Comment on the morphology of the red blood cells.
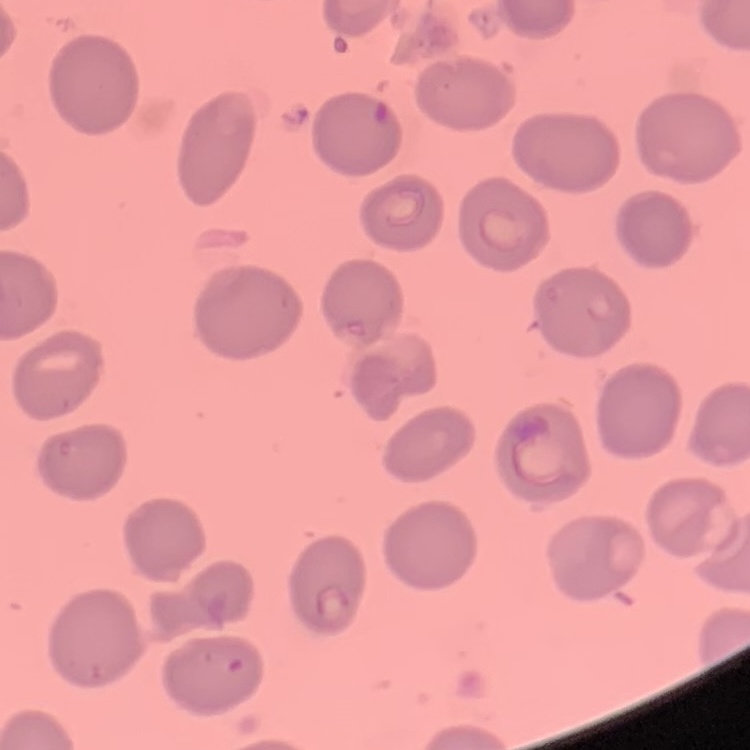

No rouleaux formation.

preparation: thin blood smear
stain: Field's or Giemsa
image_type: square crop of a larger photomicrograph